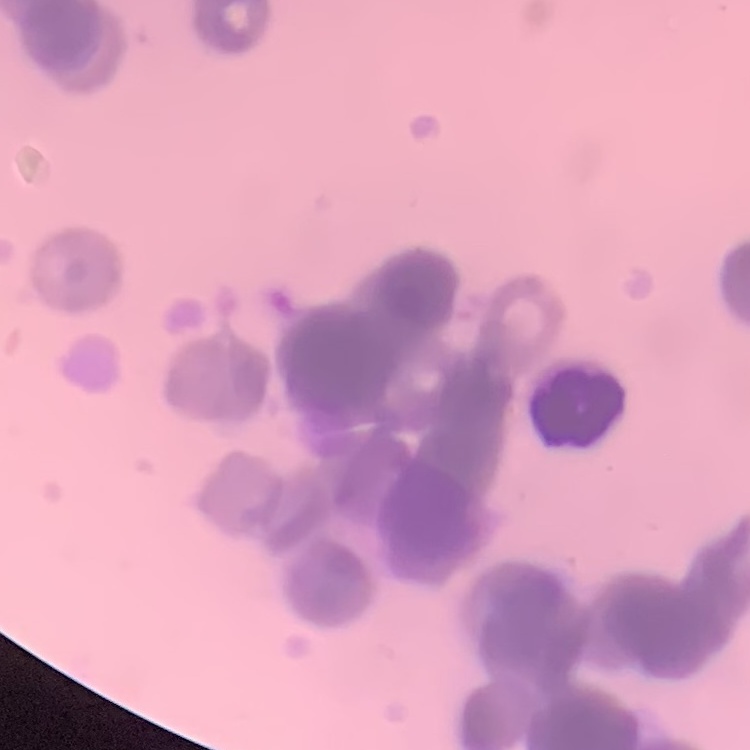
red_blood_cell_morphology: rouleaux formation
image_type: square crop of a larger photomicrograph
preparation: thin blood smear
stain: Field's or Giemsa